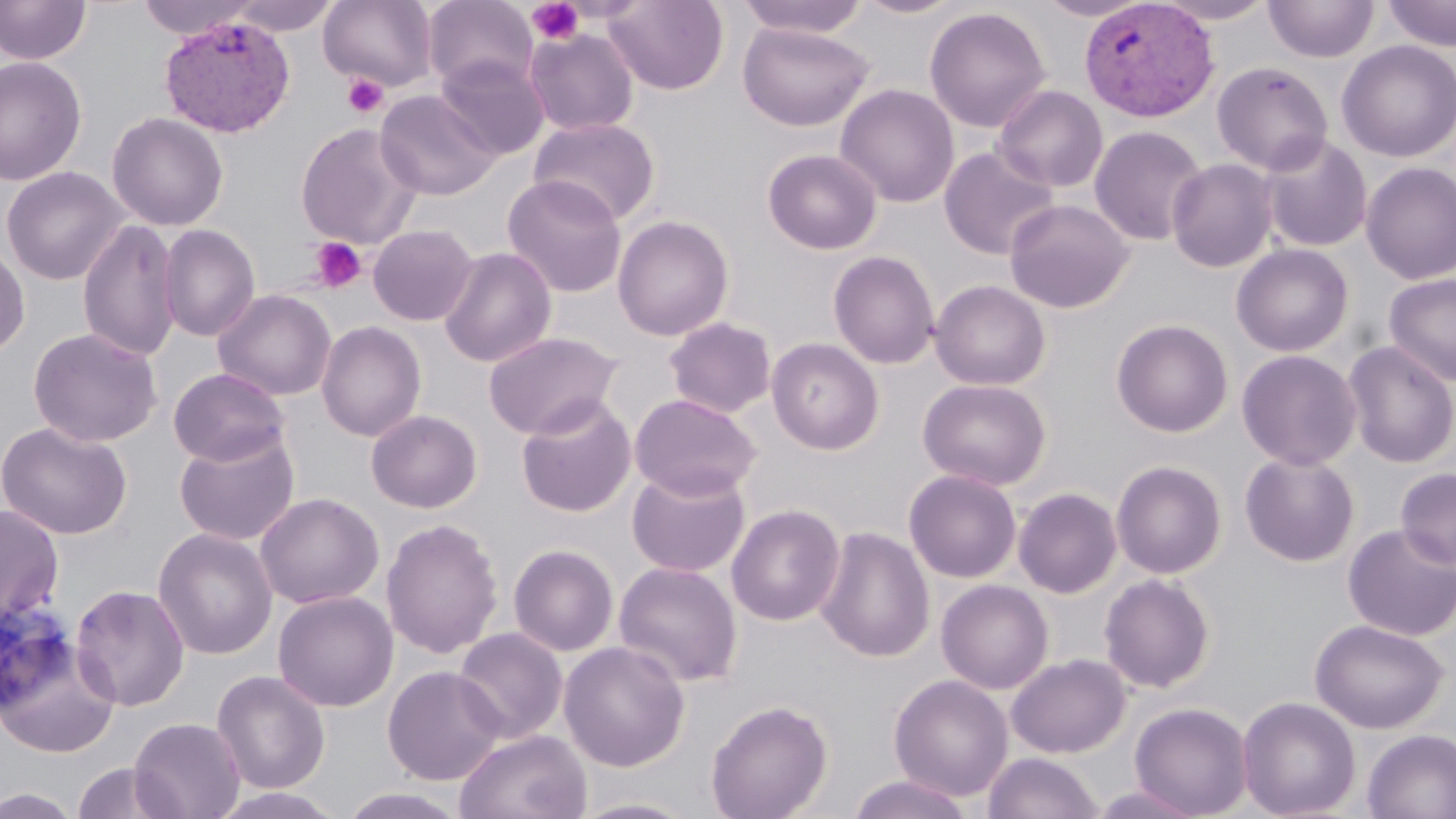
Summary:
  - Coordinate format: approximate bounding boxes as named x1/y1/x2/y2 corners in pixels
  - Platelet locations: (x1=527, y1=0, x2=584, y2=45), (x1=341, y1=73, x2=389, y2=118), (x1=309, y1=236, x2=367, y2=294)
  - Plasmodium vivax-infected red blood cell locations: (x1=1079, y1=0, x2=1218, y2=121), (x1=159, y1=15, x2=296, y2=138)
  - Uninfected red blood cell locations: (x1=0, y1=0, x2=92, y2=65), (x1=134, y1=0, x2=263, y2=39), (x1=225, y1=0, x2=341, y2=36), (x1=318, y1=0, x2=438, y2=92), (x1=422, y1=0, x2=538, y2=93), (x1=603, y1=0, x2=729, y2=95), (x1=733, y1=0, x2=872, y2=38), (x1=853, y1=0, x2=966, y2=19), (x1=1035, y1=0, x2=1152, y2=22), (x1=1153, y1=0, x2=1278, y2=24), (x1=1265, y1=0, x2=1378, y2=63), (x1=1383, y1=0, x2=1456, y2=51), (x1=923, y1=6, x2=1052, y2=133), (x1=738, y1=23, x2=875, y2=131), (x1=524, y1=28, x2=639, y2=137), (x1=1336, y1=40, x2=1456, y2=162), (x1=435, y1=54, x2=549, y2=160), (x1=0, y1=56, x2=88, y2=187), (x1=1211, y1=61, x2=1334, y2=175), (x1=835, y1=83, x2=960, y2=208), (x1=993, y1=85, x2=1108, y2=192), (x1=375, y1=89, x2=501, y2=201), (x1=107, y1=112, x2=228, y2=231), (x1=529, y1=116, x2=661, y2=226), (x1=294, y1=122, x2=423, y2=249), (x1=1089, y1=125, x2=1209, y2=246), (x1=1259, y1=135, x2=1373, y2=253), (x1=939, y1=146, x2=1060, y2=261), (x1=762, y1=148, x2=883, y2=255), (x1=1167, y1=158, x2=1278, y2=272), (x1=1360, y1=161, x2=1456, y2=285), (x1=1, y1=166, x2=128, y2=286), (x1=502, y1=175, x2=628, y2=298), (x1=1004, y1=199, x2=1135, y2=314), (x1=612, y1=214, x2=735, y2=341), (x1=77, y1=218, x2=181, y2=362), (x1=158, y1=224, x2=260, y2=342), (x1=367, y1=224, x2=478, y2=326), (x1=0, y1=240, x2=30, y2=361), (x1=1230, y1=243, x2=1354, y2=356), (x1=439, y1=246, x2=557, y2=367), (x1=828, y1=250, x2=940, y2=369), (x1=1382, y1=273, x2=1456, y2=387), (x1=930, y1=279, x2=1051, y2=391), (x1=212, y1=288, x2=336, y2=401), (x1=663, y1=316, x2=777, y2=419), (x1=1111, y1=318, x2=1233, y2=438), (x1=316, y1=320, x2=426, y2=441), (x1=27, y1=327, x2=162, y2=447), (x1=483, y1=331, x2=621, y2=439), (x1=767, y1=338, x2=884, y2=455), (x1=1342, y1=340, x2=1456, y2=468), (x1=1237, y1=349, x2=1361, y2=470), (x1=168, y1=368, x2=290, y2=467), (x1=917, y1=378, x2=1051, y2=490), (x1=630, y1=393, x2=761, y2=501), (x1=515, y1=395, x2=637, y2=518), (x1=366, y1=409, x2=482, y2=513), (x1=1, y1=420, x2=133, y2=540), (x1=174, y1=429, x2=300, y2=546), (x1=1239, y1=451, x2=1360, y2=567), (x1=1111, y1=460, x2=1227, y2=579), (x1=627, y1=466, x2=750, y2=578), (x1=1395, y1=467, x2=1456, y2=569), (x1=903, y1=469, x2=1022, y2=583), (x1=1012, y1=479, x2=1227, y2=588), (x1=1013, y1=487, x2=1122, y2=598), (x1=255, y1=492, x2=384, y2=609), (x1=0, y1=503, x2=65, y2=626), (x1=726, y1=503, x2=846, y2=626), (x1=380, y1=517, x2=504, y2=659), (x1=1342, y1=523, x2=1456, y2=642), (x1=815, y1=525, x2=935, y2=663), (x1=153, y1=528, x2=277, y2=660), (x1=508, y1=544, x2=619, y2=656), (x1=613, y1=561, x2=743, y2=687), (x1=1098, y1=572, x2=1216, y2=693), (x1=936, y1=579, x2=1054, y2=694), (x1=70, y1=584, x2=190, y2=712), (x1=272, y1=590, x2=399, y2=712), (x1=1310, y1=619, x2=1449, y2=734), (x1=453, y1=627, x2=567, y2=744), (x1=0, y1=635, x2=122, y2=758), (x1=558, y1=640, x2=691, y2=771), (x1=1006, y1=653, x2=1131, y2=758), (x1=382, y1=665, x2=506, y2=785), (x1=211, y1=670, x2=331, y2=795), (x1=888, y1=674, x2=1013, y2=801), (x1=1237, y1=696, x2=1361, y2=818), (x1=705, y1=698, x2=834, y2=819), (x1=1129, y1=701, x2=1253, y2=818), (x1=129, y1=717, x2=245, y2=819), (x1=454, y1=729, x2=592, y2=819), (x1=1361, y1=729, x2=1456, y2=819), (x1=982, y1=752, x2=1104, y2=819), (x1=70, y1=762, x2=184, y2=819), (x1=847, y1=774, x2=975, y2=819), (x1=1087, y1=785, x2=1206, y2=819), (x1=1, y1=787, x2=85, y2=818), (x1=336, y1=788, x2=470, y2=818), (x1=566, y1=795, x2=702, y2=818)
  - Slide-level diagnosis: Plasmodium vivax
  - Stain: May-Grünwald-Giemsa
  - Field of view: one of a larger specimen
  - Preparation: thin blood film
  - Image size: 1456×819 pixels
  - Modality: optical microscopy
  - Magnification: 1000x